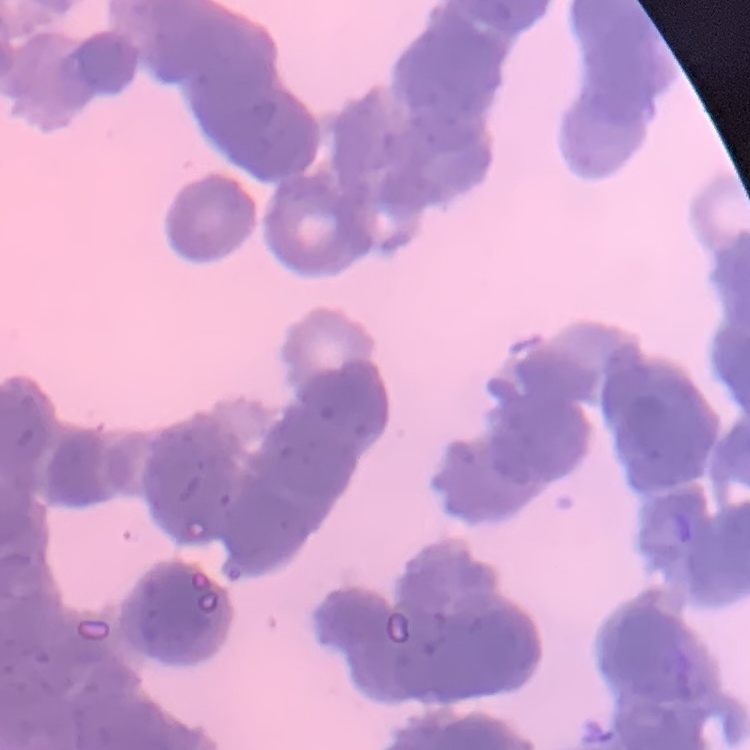

erythrocyte morphology = rouleaux formation
stain = Field's or Giemsa
preparation = thin blood smear
image type = one tile cut from a larger photomicrograph